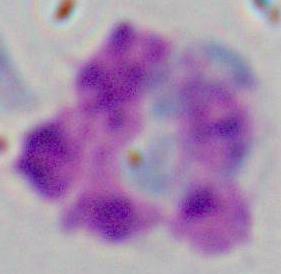
Summary:
  - Modality: photomicrograph
  - Magnification: 1000x
  - Identification: white blood cell